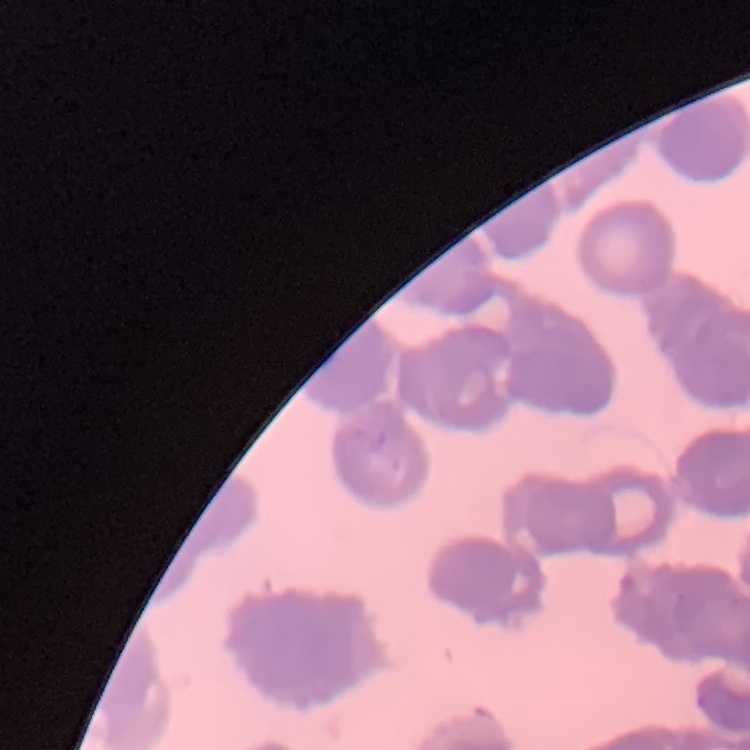

{
  "erythrocyte_morphology": "rouleaux formation",
  "image_type": "one tile cut from a larger photomicrograph",
  "preparation": "thin blood smear",
  "stain": "Field's or Giemsa"
}